Name the cell type shown.
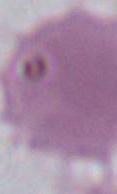

This is an erythrocyte.

1000x magnification. Photomicrograph.